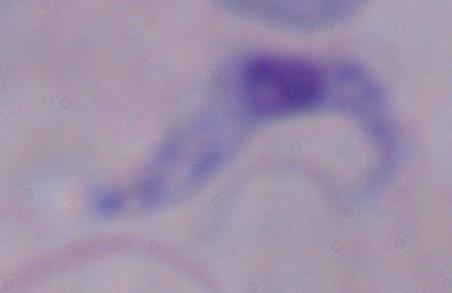 Captured at 1000x magnification. Micrograph. A trypanosome is seen.